Outline each Plasmodium ovale-infected red blood cell.
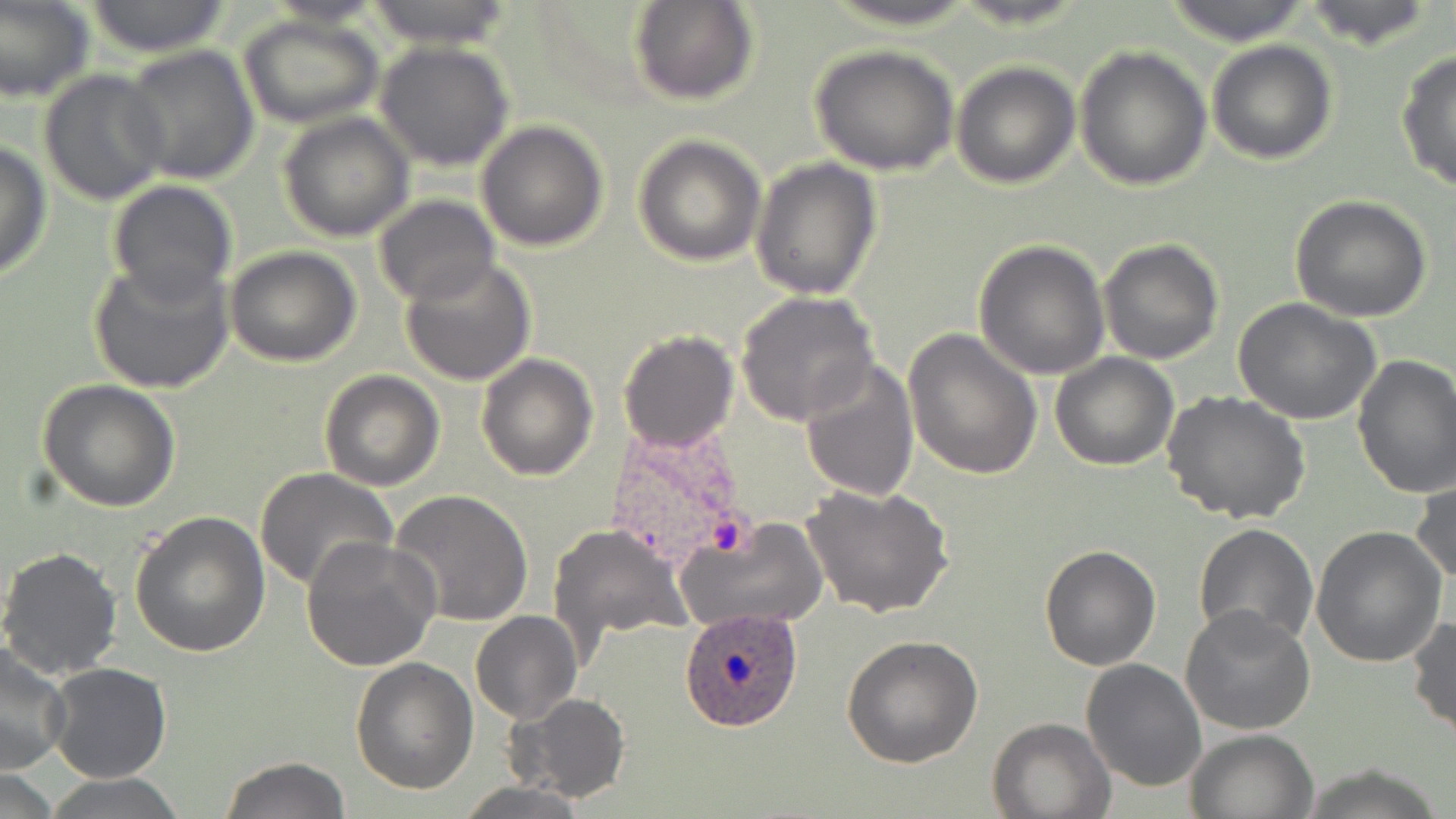

Approximate bounding boxes as (x1,y1)-(x2,y2) corner pairs in pixels.
Plasmodium ovale-infected red blood cells: (680,606)-(806,732).

Summary:
  - Uninfected red blood cell locations: (0,0)-(94,104), (82,0)-(232,56), (362,0)-(517,48), (630,0)-(760,107), (823,0)-(981,29), (1163,0)-(1314,46), (1296,0)-(1441,50), (237,14)-(384,128), (1206,40)-(1338,165), (373,41)-(516,171), (120,43)-(260,184), (811,45)-(959,175), (1073,46)-(1212,190), (1394,48)-(1456,195), (950,61)-(1081,188), (39,68)-(169,206), (279,112)-(415,242), (476,121)-(608,250), (633,134)-(767,265), (0,139)-(53,281), (750,157)-(882,300), (106,180)-(238,303), (372,195)-(500,306), (1291,195)-(1432,321), (1097,238)-(1224,365), (975,239)-(1112,380), (224,246)-(362,367), (399,256)-(537,387), (87,257)-(235,395), (735,292)-(880,428), (1235,299)-(1384,426), (900,327)-(1043,478), (618,328)-(739,453), (1049,351)-(1179,471), (476,353)-(600,481), (1352,354)-(1456,499), (800,360)-(919,502), (319,369)-(445,492), (37,378)-(181,512), (1163,390)-(1312,525), (254,468)-(400,593), (1411,477)-(1456,587), (801,482)-(955,618), (390,490)-(534,627), (131,509)-(271,656), (675,516)-(828,634), (1193,523)-(1318,648), (547,524)-(694,655), (1310,527)-(1447,668), (302,537)-(440,671), (1039,543)-(1161,670), (0,546)-(124,682), (1181,606)-(1315,736), (470,612)-(581,723), (1408,615)-(1456,741), (842,636)-(984,768), (0,647)-(72,775), (350,657)-(478,795), (1080,659)-(1206,793), (46,663)-(172,783), (509,692)-(631,805), (986,717)-(1113,818), (1184,729)-(1318,818), (219,756)-(352,818), (1291,763)-(1452,819), (45,773)-(188,819), (455,781)-(591,818)
  - Slide-level diagnosis: Plasmodium ovale
  - Field of view: single
  - Magnification: 1000x
  - Preparation: thin blood film
  - Image size: 1456×819 pixels
  - Stain: May-Grünwald-Giemsa
  - Modality: optical microscopy